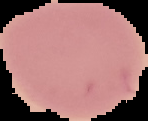

image size = 148×121 pixels
image type = segmented cell region with the area outside set to black
preparation = thin blood smear
malaria status = uninfected